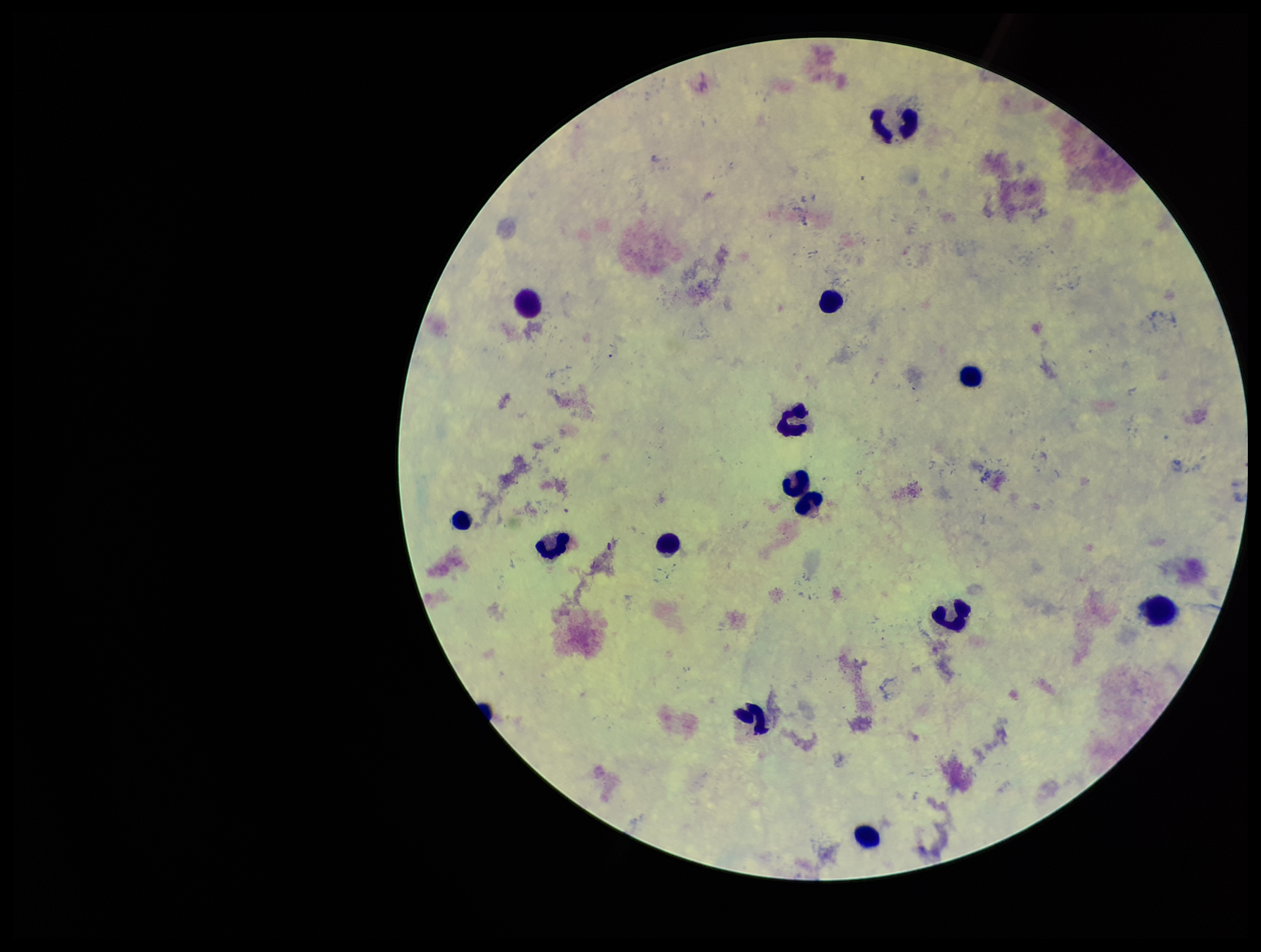

patient malaria status = negative
Plasmodium parasites = none detected
capture = smartphone photograph through the microscope eyepiece
field of view = single
parasite count = 0
leukocyte count = 14
preparation = thick smear
stain = Giemsa
image size = 1261×952 pixels